Classify this cell by malaria status.
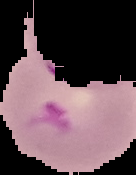

Parasitized.

preparation = thin blood smear
image size = 136×175 pixels
image type = cell region segmented out of the field of view; surrounding area masked to black